Report the malaria status of this cell.
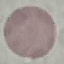

Uninfected.

preparation = thin smear
capture = smartphone camera at the microscope eyepiece
stain = Giemsa
image type = automatically extracted cell patch, resized to 64 × 64 pixels